Classify this cell by malaria status.
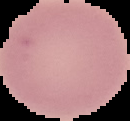

It is uninfected.

Summary:
  - Image size: 130×121 pixels
  - Preparation: thin blood smear
  - Image type: segmented cell region with the area outside set to black